Name the cell type shown.
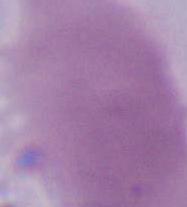

An erythrocyte.

Photomicrograph. Captured at 1000x magnification.